Classify this cell by malaria status.
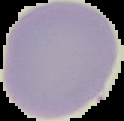
Uninfected.

preparation = thin blood film
image size = 124×121 pixels
image type = segmented cell region on a black background